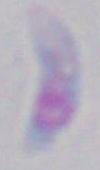

Captured at 1000x magnification. Toxoplasma gondii is shown. Photomicrograph.